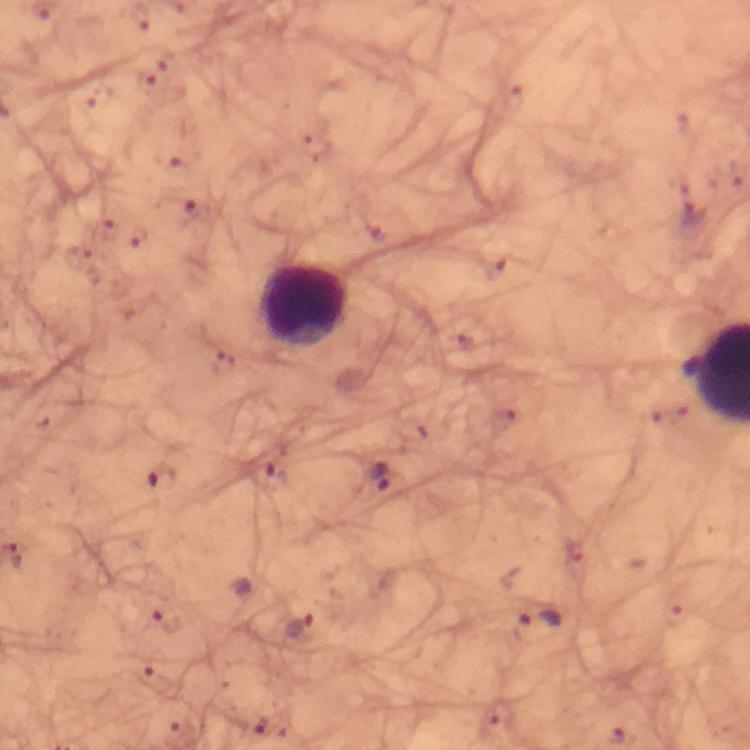

Approximate centers as {x, y} in pixels. Leukocyte locations: {306, 306}. Plasmodium parasite locations: {145, 78}, {176, 166}, {192, 211}, {692, 213}, {139, 234}, {495, 270}, {223, 365}, {381, 477}, {161, 478}, {167, 619}, {540, 621}, {300, 626}, {142, 676}. From a malaria diagnostic workup. Smartphone photograph taken through a microscope. Giemsa stain. Cropped region of a single field of view. 100x magnification. Immersion oil was used. Image is 750×750 pixels. Thick blood film.